Report the malaria status of this cell.
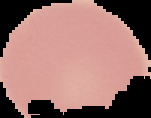
Uninfected.

{
  "preparation": "thin blood smear",
  "image_type": "segmented cell region with the area outside set to black",
  "image_size": "151×118 pixels"
}